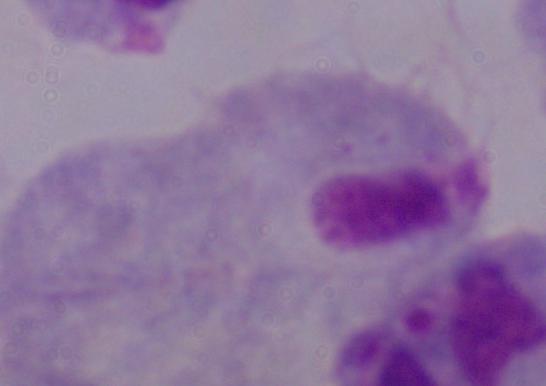

modality = photomicrograph
identification = trichomonad
magnification = 1000x